Classify this cell by malaria status.
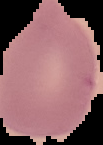
It is uninfected.

image size = 103×145 pixels
image type = cell region segmented out of the field of view; surrounding area masked to black
preparation = thin blood smear